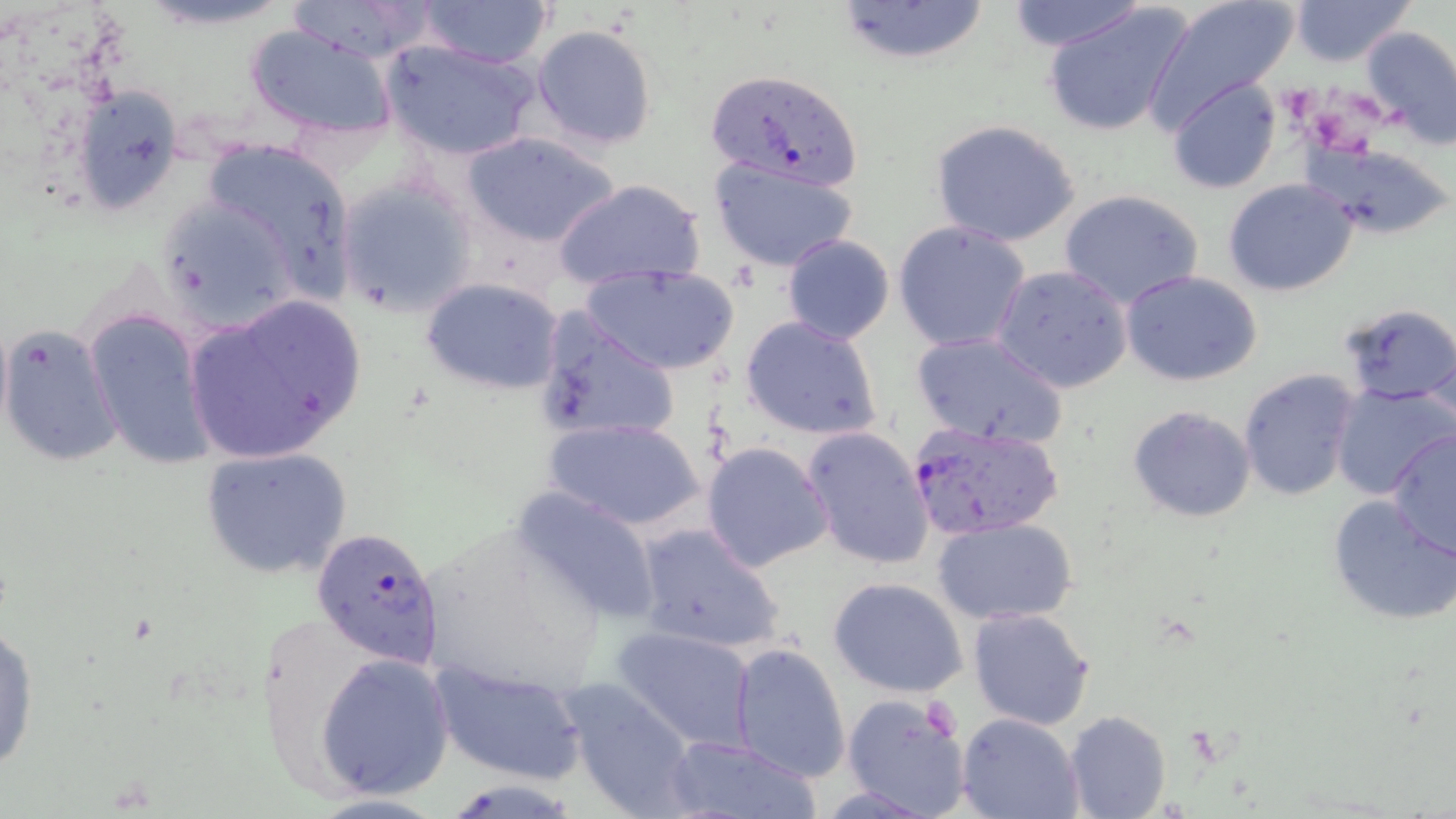

Approximate bounding boxes as named x1/y1/x2/y2 corners in pixels. Uninfected red blood cell locations: (x1=286, y1=0, x2=441, y2=66), (x1=417, y1=0, x2=555, y2=70), (x1=832, y1=0, x2=993, y2=65), (x1=1003, y1=0, x2=1153, y2=50), (x1=1148, y1=0, x2=1294, y2=122), (x1=1287, y1=0, x2=1416, y2=67), (x1=1043, y1=3, x2=1194, y2=138), (x1=244, y1=24, x2=396, y2=139), (x1=532, y1=24, x2=657, y2=151), (x1=1359, y1=25, x2=1456, y2=147), (x1=381, y1=39, x2=540, y2=162), (x1=1168, y1=78, x2=1281, y2=193), (x1=69, y1=85, x2=185, y2=215), (x1=931, y1=120, x2=1081, y2=247), (x1=460, y1=129, x2=623, y2=250), (x1=196, y1=135, x2=359, y2=307), (x1=1296, y1=139, x2=1454, y2=241), (x1=707, y1=159, x2=858, y2=273), (x1=337, y1=177, x2=478, y2=314), (x1=553, y1=177, x2=706, y2=292), (x1=1224, y1=178, x2=1359, y2=297), (x1=1057, y1=188, x2=1205, y2=310), (x1=153, y1=192, x2=306, y2=335), (x1=892, y1=221, x2=1032, y2=354), (x1=781, y1=234, x2=894, y2=344), (x1=581, y1=264, x2=741, y2=376), (x1=991, y1=265, x2=1134, y2=393), (x1=1121, y1=272, x2=1263, y2=387), (x1=421, y1=277, x2=565, y2=396), (x1=182, y1=295, x2=368, y2=466), (x1=1339, y1=303, x2=1455, y2=406), (x1=83, y1=304, x2=217, y2=472), (x1=535, y1=309, x2=681, y2=446), (x1=739, y1=315, x2=882, y2=442), (x1=0, y1=323, x2=122, y2=469), (x1=909, y1=331, x2=1067, y2=448), (x1=1422, y1=336, x2=1454, y2=447), (x1=1238, y1=369, x2=1358, y2=501), (x1=1331, y1=381, x2=1456, y2=501), (x1=1127, y1=406, x2=1256, y2=522), (x1=546, y1=417, x2=704, y2=532), (x1=802, y1=425, x2=935, y2=570), (x1=1384, y1=429, x2=1456, y2=562), (x1=702, y1=440, x2=835, y2=573), (x1=200, y1=447, x2=353, y2=579), (x1=510, y1=485, x2=664, y2=626), (x1=1326, y1=494, x2=1456, y2=627), (x1=933, y1=517, x2=1077, y2=624), (x1=413, y1=518, x2=609, y2=703), (x1=632, y1=524, x2=786, y2=653), (x1=828, y1=576, x2=968, y2=699), (x1=967, y1=606, x2=1096, y2=731), (x1=249, y1=611, x2=389, y2=803), (x1=0, y1=621, x2=39, y2=777), (x1=614, y1=625, x2=758, y2=753), (x1=729, y1=642, x2=850, y2=782), (x1=316, y1=653, x2=456, y2=798), (x1=431, y1=659, x2=585, y2=784), (x1=558, y1=680, x2=699, y2=817), (x1=841, y1=692, x2=974, y2=819), (x1=1064, y1=709, x2=1171, y2=819), (x1=956, y1=713, x2=1084, y2=819), (x1=662, y1=733, x2=821, y2=817). Plasmodium falciparum-infected red blood cell locations: (x1=702, y1=66, x2=867, y2=192), (x1=912, y1=420, x2=1066, y2=537), (x1=311, y1=526, x2=444, y2=670). Slide-level diagnosis: Plasmodium falciparum. May-Grünwald-Giemsa-stained preparation. Thin blood film. One field of a larger specimen. Light microscopy. Image is 1456×819 pixels. Captured at 1000x magnification.